State which cell type is depicted.
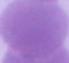

This is an erythrocyte.

magnification = 1000x
modality = photomicrograph